Assess the morphology of the red blood cells.
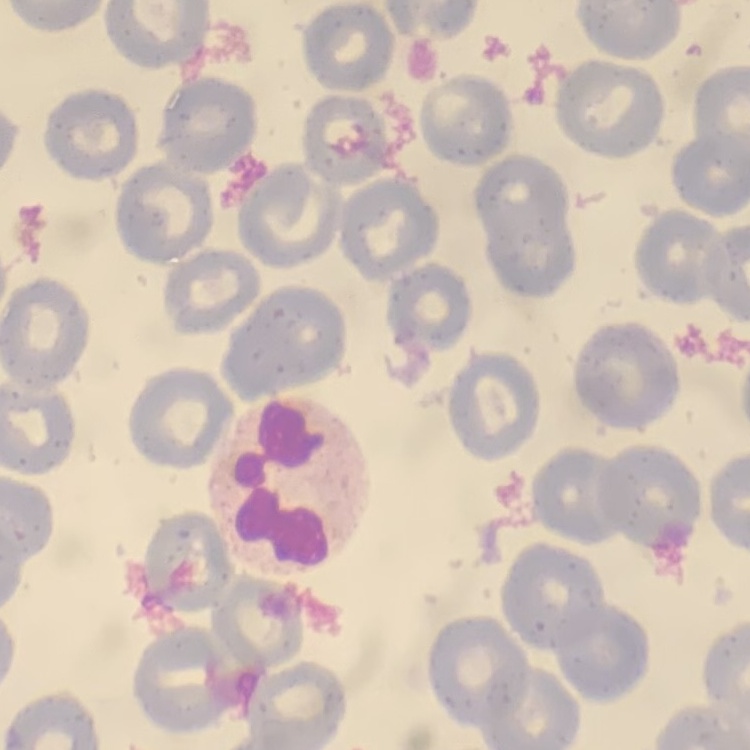

No rouleaux formation.

One tile cut from a larger photomicrograph. Field's or Giemsa stain. Thin blood smear.